Outline every malaria parasite.
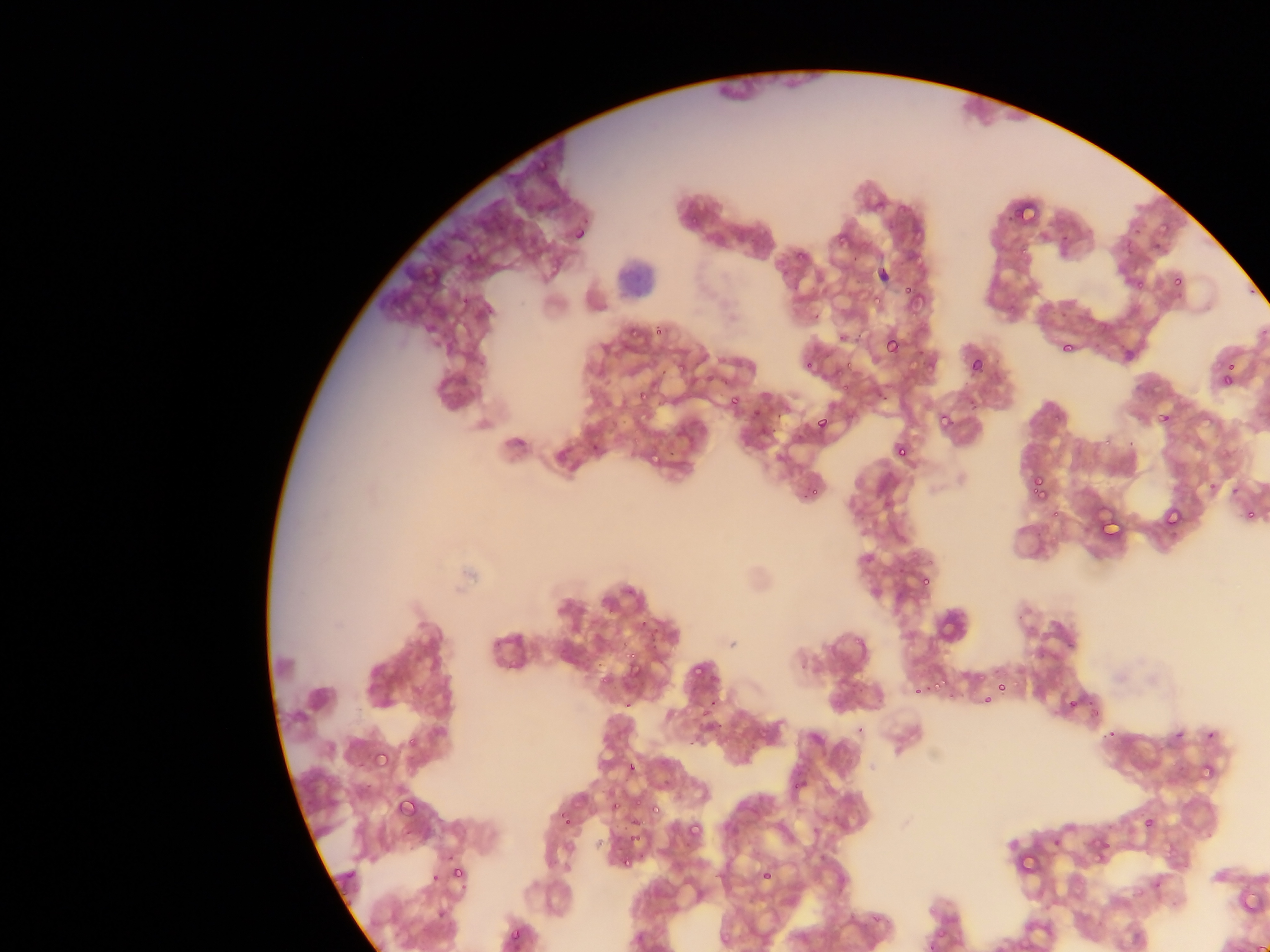

Approximate bounding boxes as left top right bottom in pixels.
Malaria parasites: 532 152 551 180; 529 192 550 212; 1012 200 1041 230; 1155 213 1181 244; 828 227 848 250; 572 231 585 239; 466 234 497 265; 1114 240 1138 261; 788 254 801 269; 543 256 571 276; 1170 271 1187 288; 896 276 911 295; 1130 280 1141 302; 858 284 890 307; 901 293 920 320; 623 325 642 349; 882 333 905 359; 1059 339 1076 356; 836 348 854 366; 966 354 987 377; 1216 359 1240 387; 801 360 824 373; 631 381 655 408; 841 382 851 392; 725 393 744 415; 1151 403 1178 427; 750 404 766 422; 935 410 956 434; 812 412 833 435; 891 440 912 465; 653 444 670 463; 1027 472 1052 502; 801 485 816 505; 1098 500 1131 535; 1244 502 1260 522; 1161 504 1186 532; 915 569 935 592; 644 633 665 659; 623 648 645 676; 687 654 710 679; 917 671 948 699; 991 679 1007 697; 970 692 987 715; 1063 693 1077 708; 371 746 394 773; 1194 764 1215 778; 785 771 804 797; 394 793 419 821; 647 801 666 822; 556 808 574 828; 1137 817 1154 832; 682 819 705 846; 1086 820 1125 856; 625 822 645 848; 1013 838 1046 883; 448 851 480 886; 617 855 640 882; 754 858 784 885; 506 924 528 948.

preparation = thin blood smear
capture = mobile-phone photograph through a microscope
field of view = single
image size = 1270×952 pixels
leukocyte locations = approximate bounding boxes as left top right bottom in pixels: 607 248 661 307
country = Ghana